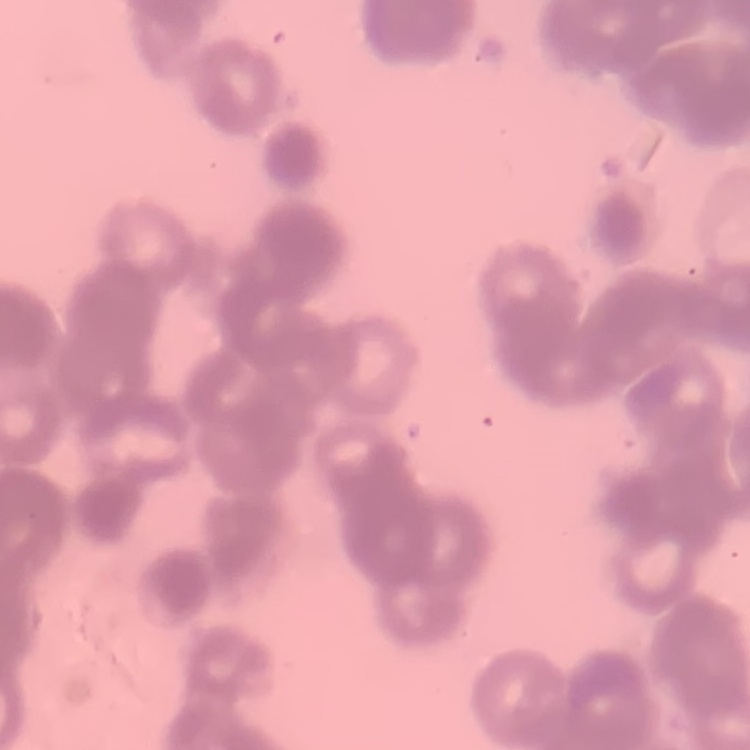

Summary:
  - Erythrocyte morphology: rouleaux formation
  - Stain: Field's or Giemsa
  - Image type: square crop of a larger photomicrograph
  - Preparation: thin peripheral smear